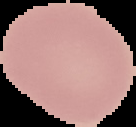
Summary:
  - Image type: cell region segmented out of the field of view; surrounding area masked to black
  - Image size: 136×127 pixels
  - Malaria status: uninfected
  - Preparation: thin blood film